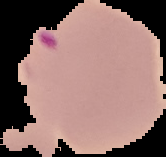 Segmented cell region on a black background. Result: Plasmodium parasites identified. Image is 166×157 pixels. From a thin blood film.